Report the malaria status of this cell.
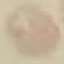

Uninfected.

{
  "image_type": "cell patch, automatically extracted from a larger field of view and resized to 64 × 64 pixels",
  "stain": "Giemsa",
  "preparation": "thin blood film",
  "capture": "smartphone through the microscope eyepiece"
}